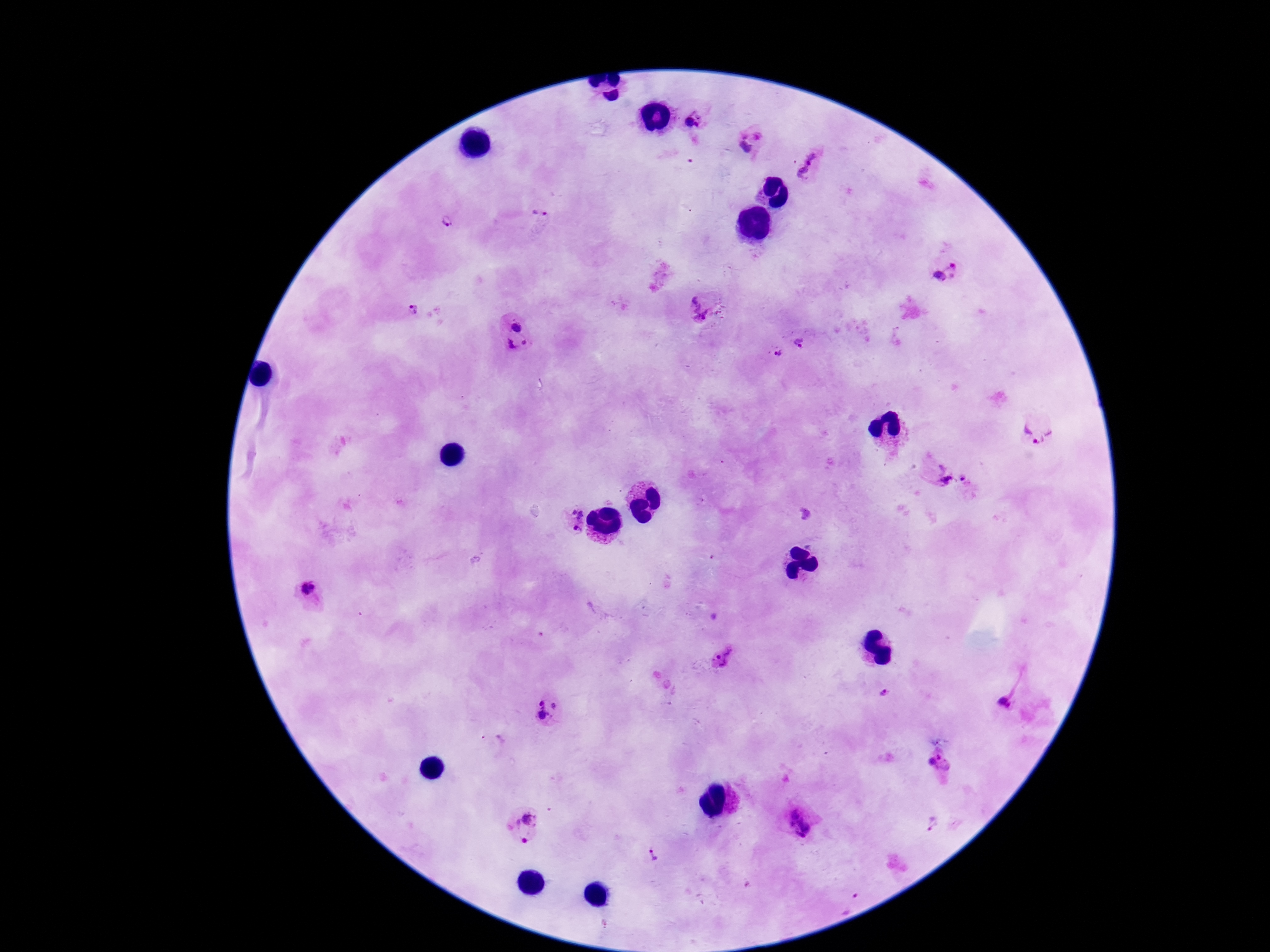

Approximate centers as {x, y} in pixels. Plasmodium parasite locations: {688, 121}, {697, 125}, {751, 129}, {745, 148}, {808, 167}, {541, 214}, {448, 223}, {948, 272}, {697, 307}, {413, 310}, {516, 327}, {524, 342}, {799, 343}, {510, 346}, {779, 353}, {1038, 429}, {942, 477}, {963, 480}, {575, 520}, {307, 591}, {726, 657}, {886, 694}, {540, 702}, {1006, 702}, {556, 705}, {543, 716}, {493, 744}, {932, 758}, {946, 766}, {799, 823}, {934, 823}, {523, 827}, {652, 857}, {850, 903}. Patient malaria status: infected. Image is 1270×952 pixels. Smartphone photograph taken through the microscope eyepiece. Thick blood film. Single field of view. Giemsa-stained preparation. 100x magnification.